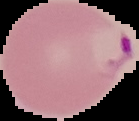

Summary:
  - Malaria status: parasitized
  - Image type: cell region segmented out of the field of view; surrounding area masked to black
  - Image size: 139×121 pixels
  - Preparation: thin blood film